Classify this cell by malaria status.
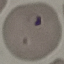

Parasitized.

Cell patch, automatically extracted from a larger field of view and resized to 64 × 64 pixels. Acquired by smartphone through the microscope eyepiece. Thin blood film. Giemsa stain.